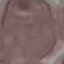 Malaria status: uninfected. Giemsa-stained preparation. Thin blood film. Acquired by smartphone through the microscope eyepiece. Automatically extracted cell patch, resized to 64 × 64 pixels.